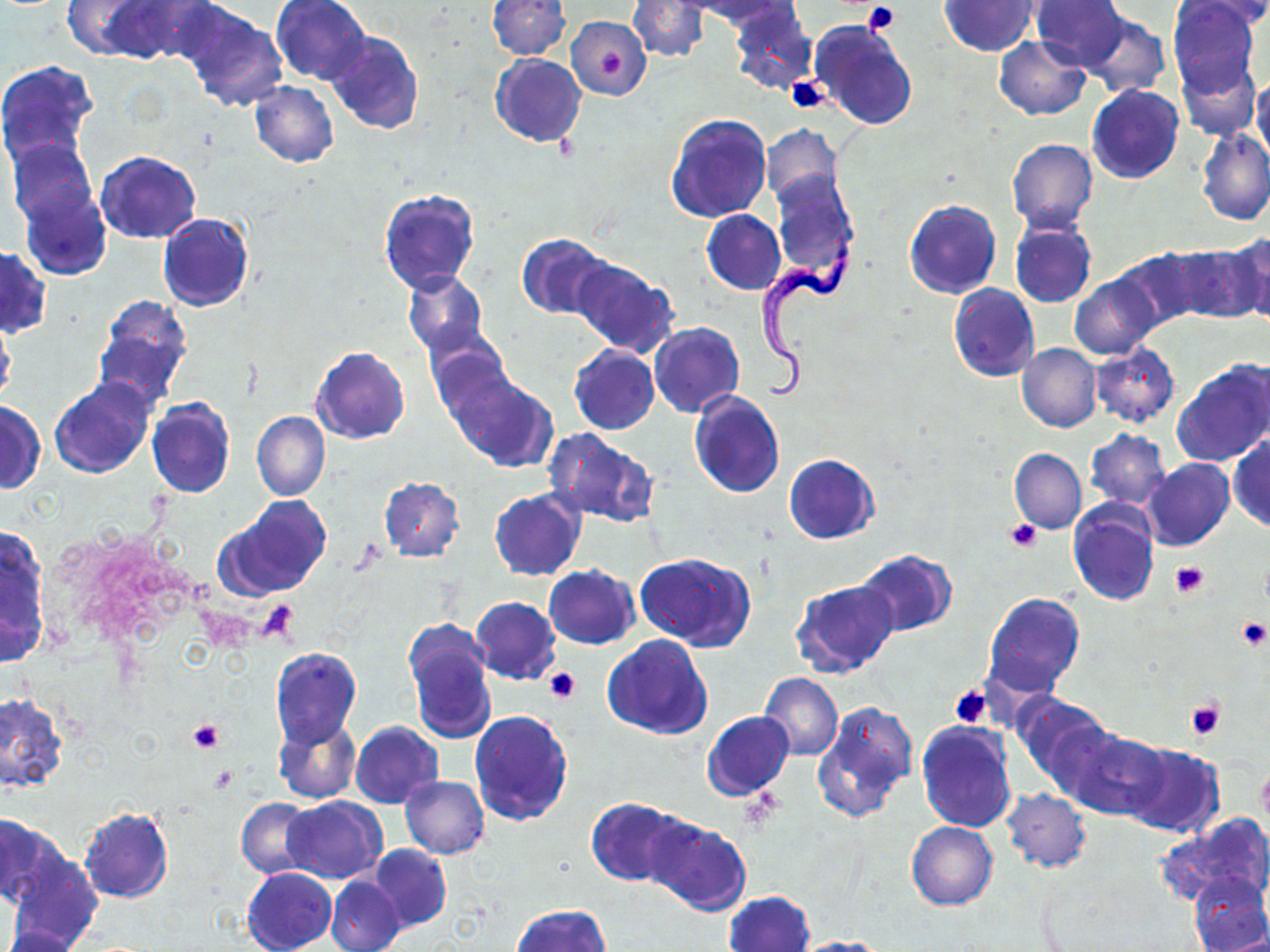 Approximate bounding boxes as [x1, y1, x2, y2] in pixels. Platelet locations: [862, 3, 901, 34], [596, 44, 627, 79], [787, 76, 829, 112], [1008, 519, 1041, 551], [1170, 562, 1209, 599], [256, 599, 299, 643], [1235, 616, 1269, 652], [544, 667, 580, 703], [950, 685, 994, 729], [1185, 697, 1226, 740], [187, 719, 224, 754]. Uninfected red blood cell locations: [63, 0, 155, 60], [92, 0, 202, 64], [272, 0, 372, 85], [485, 0, 570, 59], [628, 0, 710, 62], [684, 0, 794, 26], [941, 0, 1041, 55], [1029, 0, 1129, 72], [1167, 0, 1259, 95], [1182, 0, 1270, 28], [177, 3, 288, 113], [728, 4, 818, 95], [570, 7, 708, 80], [1079, 12, 1170, 100], [567, 16, 651, 99], [808, 19, 918, 131], [325, 31, 424, 135], [993, 36, 1091, 120], [489, 53, 586, 147], [1176, 56, 1260, 140], [0, 60, 98, 168], [1253, 75, 1270, 161], [250, 82, 339, 167], [1087, 84, 1184, 184], [665, 112, 773, 223], [762, 123, 843, 208], [1197, 130, 1270, 225], [8, 138, 96, 226], [1006, 139, 1097, 233], [96, 150, 201, 243], [769, 173, 858, 284], [20, 187, 111, 280], [378, 189, 480, 294], [904, 200, 1001, 299], [702, 209, 784, 294], [157, 213, 254, 312], [1010, 220, 1097, 311], [1232, 232, 1270, 326], [516, 233, 613, 321], [1165, 242, 1266, 325], [1, 246, 51, 336], [1111, 247, 1204, 332], [572, 258, 678, 357], [403, 270, 488, 356], [1069, 274, 1161, 359], [948, 284, 1038, 383], [93, 295, 194, 407], [0, 320, 17, 408], [648, 322, 744, 417], [425, 332, 515, 426], [1017, 343, 1101, 432], [1089, 344, 1181, 428], [311, 346, 410, 444], [569, 346, 659, 434], [1173, 357, 1270, 466], [448, 371, 557, 471], [49, 378, 155, 478], [689, 390, 785, 499], [148, 398, 236, 498], [0, 402, 45, 493], [252, 412, 330, 501], [544, 429, 659, 526], [1085, 429, 1171, 509], [1228, 433, 1270, 533], [1010, 449, 1085, 533], [784, 453, 879, 544], [1140, 458, 1235, 552], [379, 476, 465, 562], [488, 489, 586, 581], [224, 496, 330, 595], [1067, 501, 1160, 606], [0, 532, 49, 667], [854, 550, 958, 638], [635, 552, 756, 650], [544, 564, 639, 649], [790, 579, 900, 679], [982, 591, 1086, 697], [470, 597, 561, 684], [405, 628, 498, 744], [602, 635, 713, 740], [270, 648, 361, 749], [759, 674, 843, 761], [1011, 692, 1112, 785], [0, 693, 67, 791], [814, 701, 918, 822], [470, 709, 573, 827], [701, 711, 795, 802], [274, 717, 362, 803], [351, 721, 443, 807], [916, 722, 1017, 832], [1057, 725, 1166, 819], [1121, 744, 1225, 839], [400, 776, 490, 858], [1003, 788, 1091, 874], [282, 796, 385, 884], [587, 796, 683, 886], [237, 797, 314, 878], [79, 806, 175, 904], [1158, 813, 1270, 908], [0, 814, 59, 907], [642, 814, 751, 916], [905, 821, 998, 910], [369, 844, 451, 933], [4, 852, 103, 950], [242, 867, 337, 952], [1187, 873, 1268, 952], [327, 876, 406, 952], [725, 891, 815, 952], [513, 905, 610, 952], [0, 926, 87, 952], [789, 936, 891, 951]. Trypanosoma brucei locations: [759, 223, 861, 399]. Slide-level diagnosis: Trypanosoma brucei. May-Grünwald-Giemsa-stained preparation. Image is 1270×952 pixels. One field of a larger specimen. Captured at 1000x magnification. Light microscopy. Thin blood film.